Comment on the morphology of the erythrocytes.
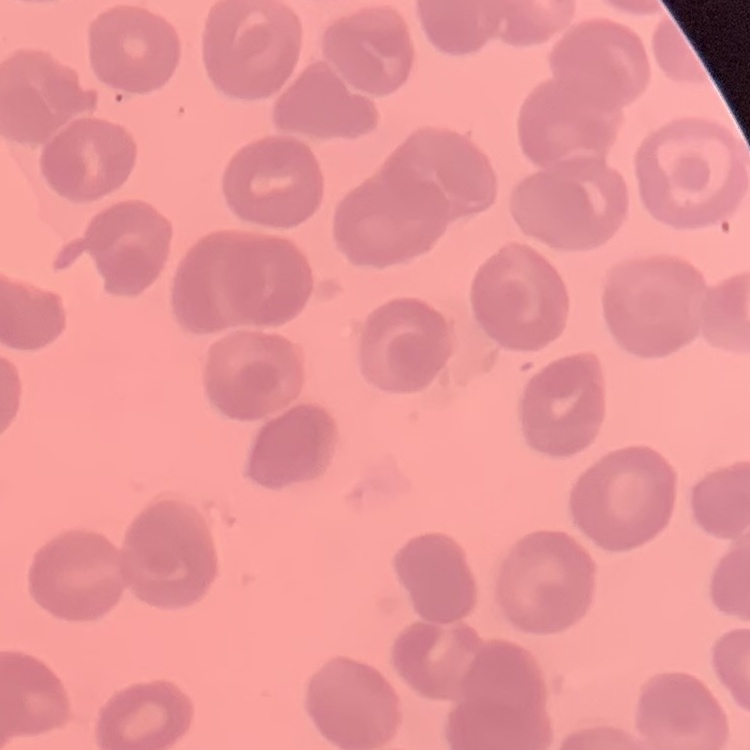
They show no rouleaux formation.

Stained with either Field's or Giemsa. Thin peripheral smear. Square crop of a larger photomicrograph.